Name the cell type shown.
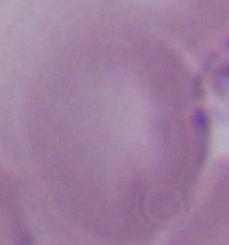

This is an erythrocyte.

modality = micrograph
magnification = 1000x